Locate every blood parasite and identify its species.
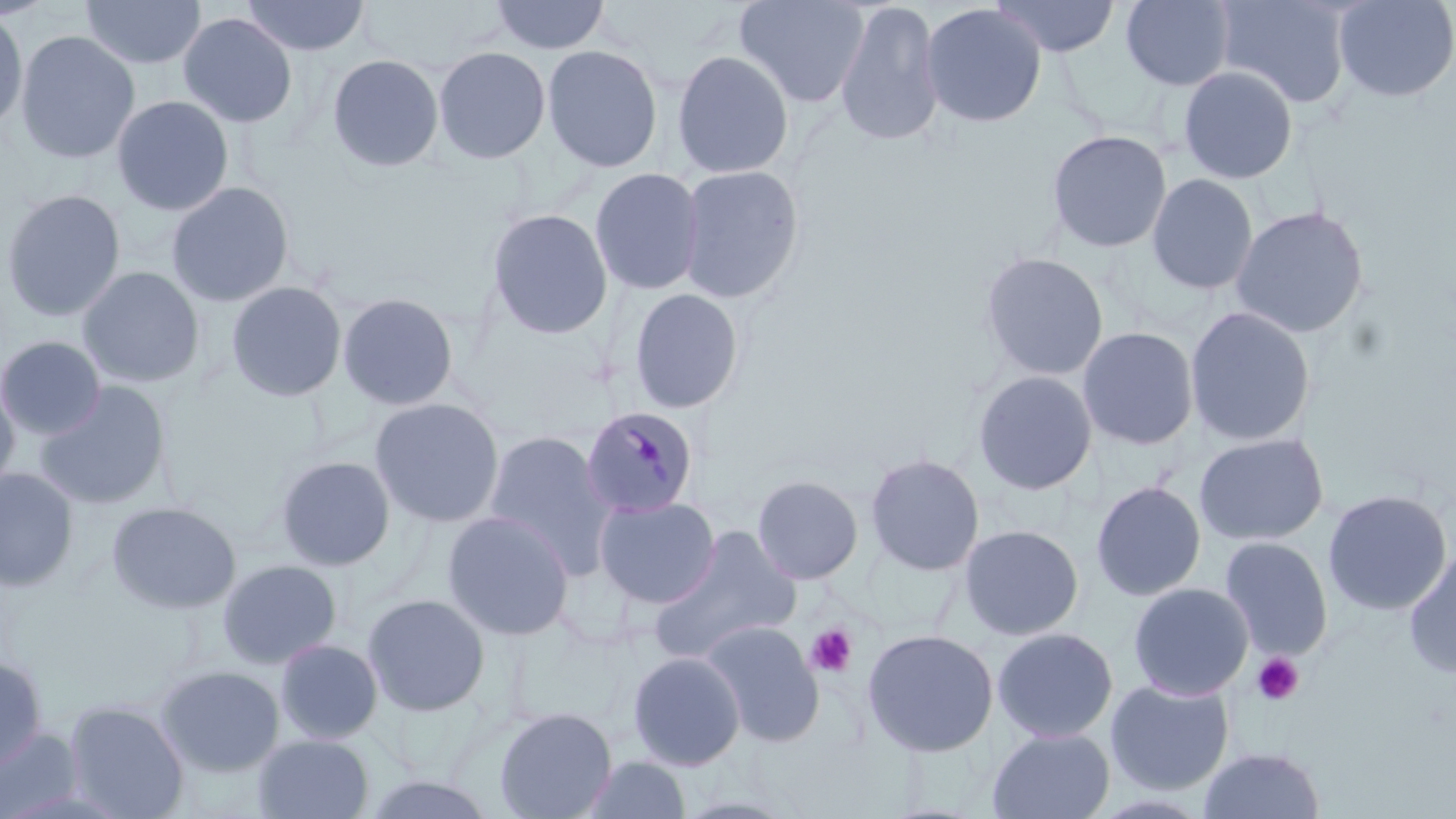

Approximate bounding boxes as [x1, y1, x2, y2] in pixels.
Plasmodium malariae-infected red blood cells: [580, 405, 699, 518].
No Plasmodium falciparum, Plasmodium ovale, Plasmodium vivax, Babesia divergens, or Trypanosoma brucei observed.

Platelet locations: [805, 623, 858, 678], [1252, 652, 1304, 705]. Uninfected red blood cell locations: [79, 0, 206, 69], [240, 0, 371, 57], [490, 0, 611, 55], [735, 0, 870, 108], [833, 0, 946, 148], [989, 0, 1121, 59], [1120, 0, 1236, 91], [1214, 0, 1354, 110], [1332, 0, 1456, 103], [920, 3, 1047, 129], [0, 8, 29, 137], [177, 12, 298, 128], [15, 30, 140, 164], [542, 44, 664, 173], [433, 45, 551, 164], [671, 49, 795, 179], [327, 53, 445, 172], [1177, 65, 1298, 184], [111, 95, 234, 216], [1046, 129, 1172, 253], [676, 164, 805, 304], [589, 168, 705, 295], [1146, 173, 1259, 295], [166, 181, 295, 307], [0, 189, 126, 322], [1230, 205, 1370, 339], [486, 207, 613, 340], [979, 251, 1109, 381], [77, 266, 205, 389], [226, 281, 348, 402], [627, 287, 745, 414], [337, 292, 459, 411], [1184, 305, 1317, 448], [1077, 325, 1200, 451], [0, 336, 107, 440], [972, 369, 1097, 495], [0, 378, 20, 498], [34, 381, 172, 511], [369, 397, 505, 528], [483, 430, 617, 573], [1193, 432, 1329, 546], [864, 452, 984, 577], [274, 455, 396, 571], [0, 467, 79, 592], [751, 474, 864, 585], [1090, 480, 1207, 601], [1322, 489, 1452, 616], [593, 494, 721, 608], [106, 502, 242, 614], [441, 510, 576, 641], [958, 524, 1084, 641], [650, 526, 803, 661], [1219, 536, 1334, 660], [1403, 546, 1456, 678], [216, 558, 343, 669], [1128, 582, 1253, 701], [361, 593, 491, 717], [700, 620, 825, 747], [992, 626, 1119, 743], [862, 628, 999, 757], [274, 638, 384, 745], [627, 651, 746, 770], [0, 655, 48, 771], [156, 665, 286, 776], [1105, 678, 1234, 796], [64, 700, 190, 819], [493, 706, 618, 819], [0, 727, 86, 818], [986, 727, 1115, 819], [252, 733, 375, 819], [1198, 747, 1326, 819], [579, 755, 692, 818], [359, 772, 501, 817]. Slide-level diagnosis: Plasmodium malariae. Image is 1456×819 pixels. 1000x magnification. May-Grünwald-Giemsa stain. Light microscopy. Single field of view. Thin blood smear.